Give the position of every Plasmodium parasite visible.
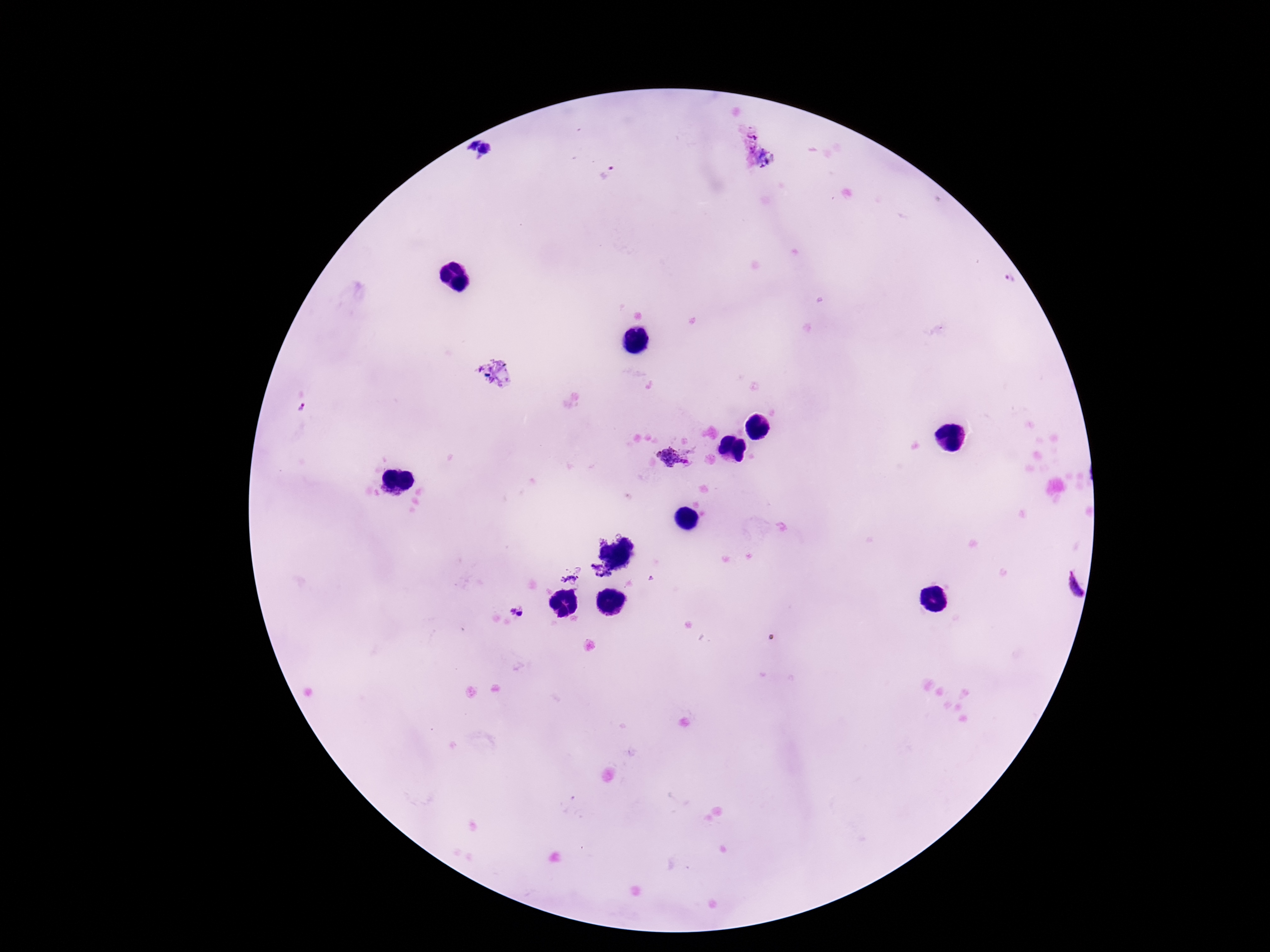
Approximate object centers, in pixels from the top-left corner.
Plasmodium parasites: (x=471, y=144), (x=488, y=150), (x=608, y=172), (x=1010, y=280), (x=301, y=409), (x=672, y=459), (x=599, y=573), (x=569, y=580), (x=1071, y=586).

Photographed through the microscope eyepiece with a smartphone camera. Thick peripheral-blood smear. Patient malaria status: positive. 100x magnification. Giemsa stain. Image is 1270×952 pixels. One field from this slide.